Report the malaria status of this cell.
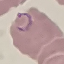
Parasitized.

Summary:
  - Image type: automatically extracted cell patch, resized to 64 × 64 pixels
  - Stain: Giemsa
  - Preparation: thin blood smear
  - Capture: smartphone through the microscope eyepiece